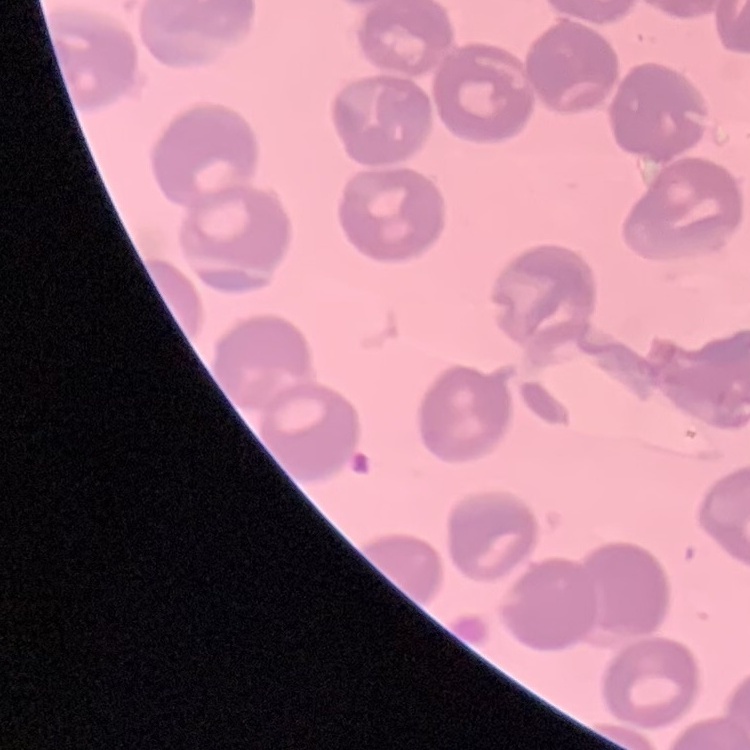 The red blood cells show no rouleaux formation. Square crop of a larger photomicrograph. Field's or Giemsa stain. Thin peripheral smear.